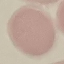

Summary:
  - Malaria status: uninfected
  - Image type: cell patch, automatically extracted from a larger field of view and resized to 64 × 64 pixels
  - Capture: smartphone through the microscope eyepiece
  - Stain: Giemsa
  - Preparation: thin blood smear